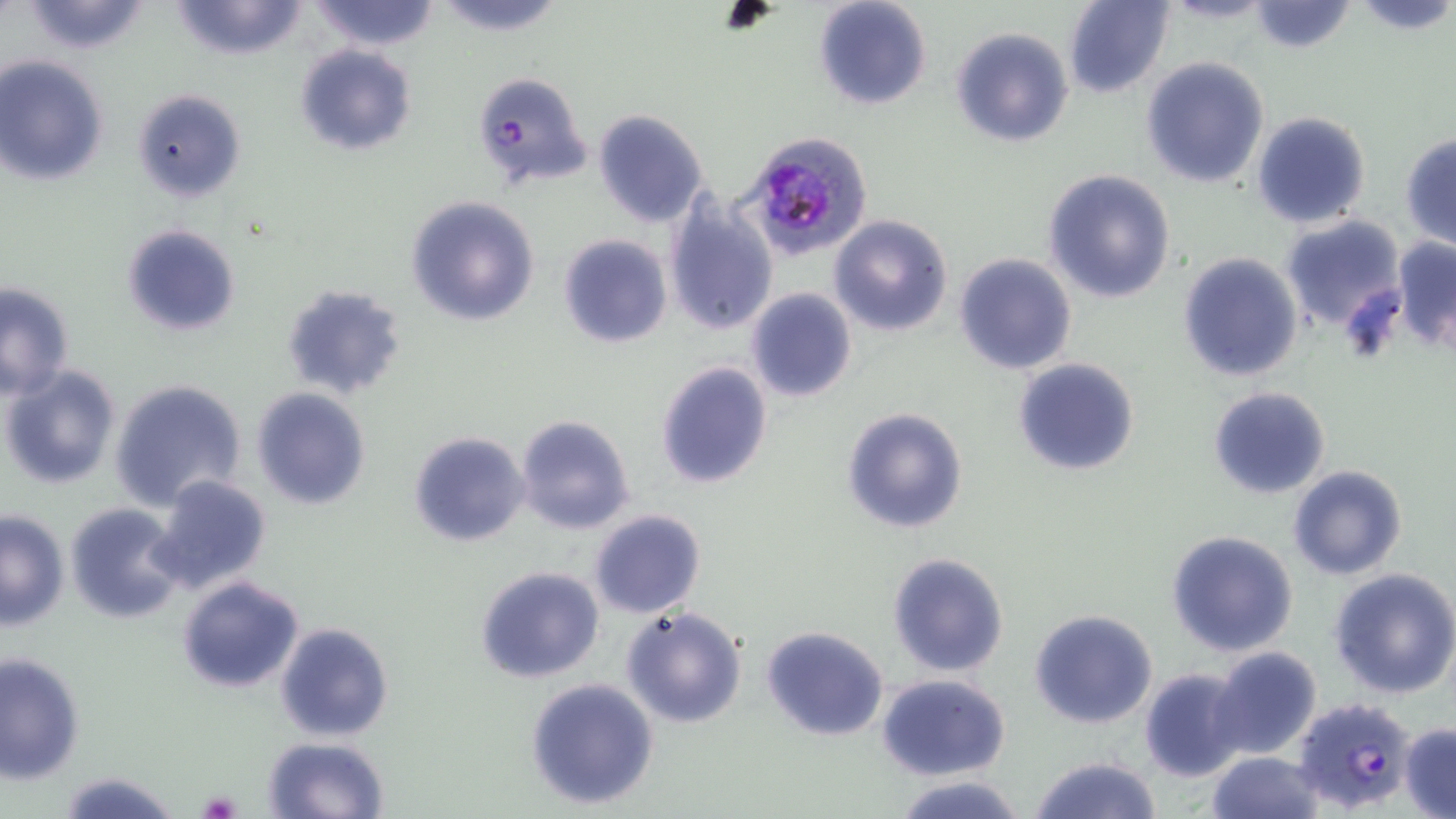

{
  "slide_level_diagnosis": "Plasmodium falciparum",
  "image_size": "1456×819 pixels",
  "stain": "May-Grünwald-Giemsa",
  "field_of_view": "single",
  "modality": "optical microscopy",
  "magnification": "1000x",
  "preparation": "thin blood film",
  "uninfected_red_blood_cell_locations": "approximate bounding boxes as (x1, y1, x2, y2) in pixels: (18, 0, 154, 54), (167, 0, 312, 61), (309, 0, 438, 51), (812, 0, 933, 112), (1063, 0, 1174, 97), (1345, 0, 1456, 33), (432, 1, 569, 35), (1245, 1, 1358, 54), (949, 27, 1074, 147), (294, 44, 417, 155), (0, 56, 109, 185), (1140, 57, 1271, 189), (473, 72, 593, 192), (130, 88, 246, 203), (591, 109, 708, 227), (1250, 110, 1372, 229), (1400, 133, 1456, 251), (1044, 168, 1177, 304), (406, 196, 540, 327), (663, 198, 779, 338), (830, 214, 952, 336), (1279, 215, 1406, 333), (120, 223, 241, 338), (558, 234, 671, 348), (1391, 235, 1456, 352), (1177, 252, 1304, 382), (952, 253, 1077, 375), (0, 281, 74, 398), (283, 283, 406, 400), (745, 288, 857, 403), (1013, 357, 1140, 477), (655, 361, 773, 491), (1, 365, 122, 490), (110, 377, 248, 511), (250, 386, 372, 509), (1206, 386, 1331, 499), (840, 407, 969, 535), (513, 414, 635, 535), (408, 430, 529, 546), (1286, 465, 1410, 581), (149, 474, 272, 592), (66, 503, 184, 623), (588, 509, 706, 618), (1, 510, 69, 629), (1165, 529, 1300, 659), (886, 551, 1010, 678), (474, 566, 604, 683), (1329, 567, 1456, 700), (176, 575, 305, 693), (621, 605, 748, 730), (1029, 608, 1160, 729), (275, 621, 394, 740), (760, 625, 889, 743), (1211, 647, 1323, 763), (0, 651, 85, 786), (1139, 667, 1248, 781), (876, 673, 1012, 781), (524, 677, 660, 810), (1399, 724, 1456, 816), (263, 736, 390, 819), (1207, 752, 1323, 819), (1028, 754, 1165, 819), (58, 772, 182, 819), (893, 774, 1031, 819)",
  "platelet_locations": "approximate bounding boxes as (x1, y1, x2, y2) in pixels: (715, 5, 781, 35), (1341, 287, 1406, 366), (198, 789, 241, 817)",
  "plasmodium_falciparum_infected_red_blood_cell_locations": "approximate bounding boxes as (x1, y1, x2, y2) in pixels: (744, 133, 875, 264), (1291, 696, 1419, 812)"
}